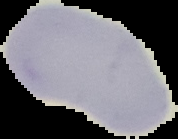
Summary:
  - Image type: cell region segmented out of the field of view; surrounding area masked to black
  - Image size: 178×139 pixels
  - Preparation: thin blood smear
  - Malaria status: uninfected